Classify this cell by malaria status.
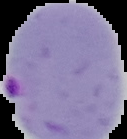

It is parasitized.

{
  "image_type": "segmented cell region on a black background",
  "image_size": "127×139 pixels",
  "preparation": "thin blood film"
}